Locate and identify every blood parasite.
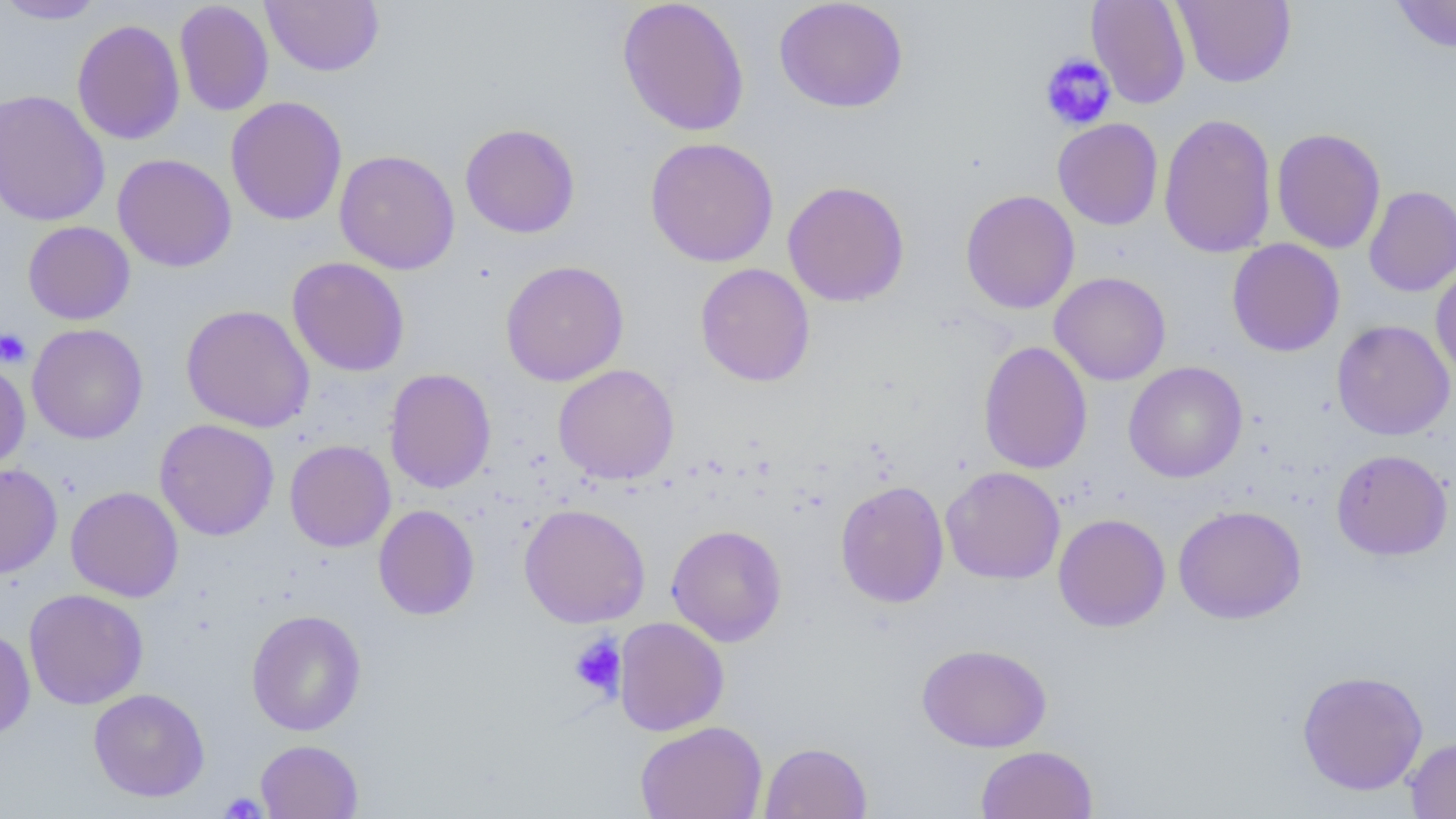

No blood parasites seen.

Summary:
  - Coordinate format: approximate bounding boxes as [x1, y1, x2, y2] in pixels
  - Uninfected red blood cell locations: [0, 0, 108, 24], [174, 0, 274, 116], [261, 0, 384, 76], [616, 0, 750, 137], [773, 0, 908, 113], [1086, 0, 1191, 109], [1173, 0, 1296, 88], [1391, 0, 1456, 53], [72, 18, 185, 145], [0, 89, 111, 227], [225, 96, 348, 226], [1158, 112, 1277, 258], [1053, 118, 1163, 230], [459, 123, 581, 239], [1271, 127, 1386, 254], [645, 137, 779, 267], [334, 149, 460, 274], [113, 153, 237, 272], [782, 180, 910, 307], [1364, 185, 1456, 297], [960, 189, 1080, 314], [23, 221, 135, 325], [1227, 239, 1345, 357], [287, 257, 410, 377], [500, 260, 629, 386], [695, 262, 815, 387], [1430, 262, 1456, 383], [1049, 271, 1171, 386], [181, 304, 315, 433], [1332, 319, 1455, 441], [26, 324, 148, 444], [978, 340, 1092, 474], [0, 358, 30, 473], [1123, 361, 1248, 483], [553, 364, 680, 485], [384, 367, 496, 494], [154, 419, 279, 541], [285, 439, 396, 552], [1331, 448, 1453, 560], [0, 463, 62, 578], [941, 466, 1066, 585], [834, 480, 949, 608], [65, 485, 184, 602], [519, 503, 650, 628], [373, 504, 480, 620], [1173, 504, 1307, 624], [1053, 513, 1171, 632], [666, 524, 787, 646], [23, 588, 149, 709], [247, 609, 366, 736], [613, 616, 729, 736], [0, 627, 35, 741], [916, 643, 1052, 752], [1296, 669, 1429, 796], [88, 688, 210, 802], [635, 721, 767, 819], [1404, 736, 1456, 818], [255, 740, 363, 818], [759, 741, 872, 818], [975, 745, 1098, 818]
  - Platelet locations: [1040, 53, 1117, 130], [0, 328, 32, 368], [569, 633, 627, 699], [219, 793, 268, 818]
  - Slide-level diagnosis: no evidence of blood parasites
  - Magnification: 1000x
  - Image size: 1456×819 pixels
  - Modality: light microscopy
  - Preparation: thin blood smear
  - Field of view: one of a larger specimen